Describe the morphology of the red blood cells.
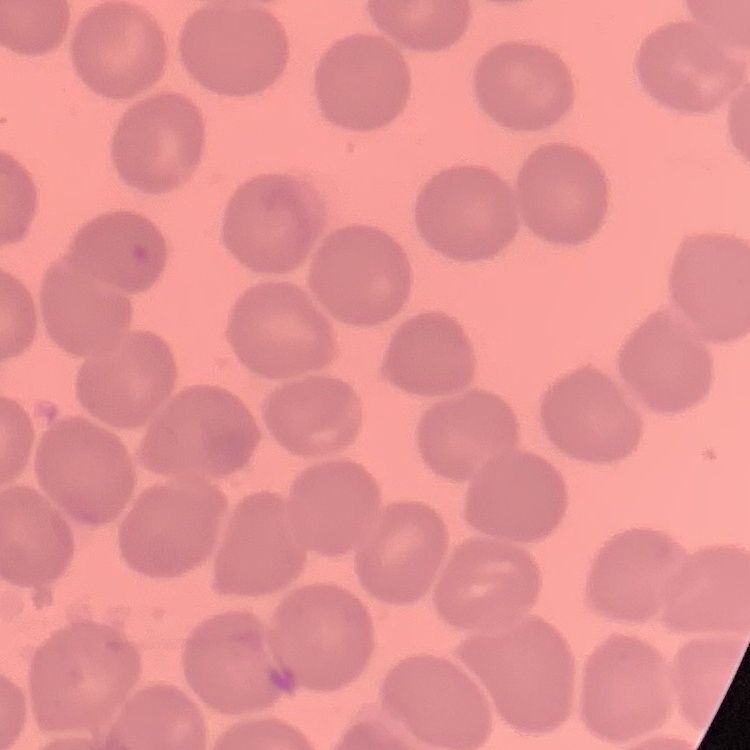

No rouleaux formation.

preparation = thin blood smear
stain = Field's or Giemsa
image type = square crop of a larger photomicrograph